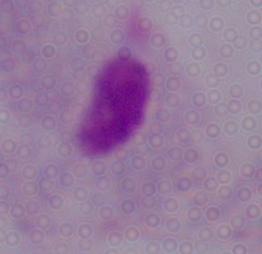

Summary:
  - Modality: micrograph
  - Magnification: 1000x
  - Identification: trichomonad